Assess this cell for malaria.
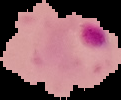
It is parasitized.

image type = cell region segmented out of the field of view; surrounding area masked to black
image size = 121×100 pixels
preparation = thin blood film